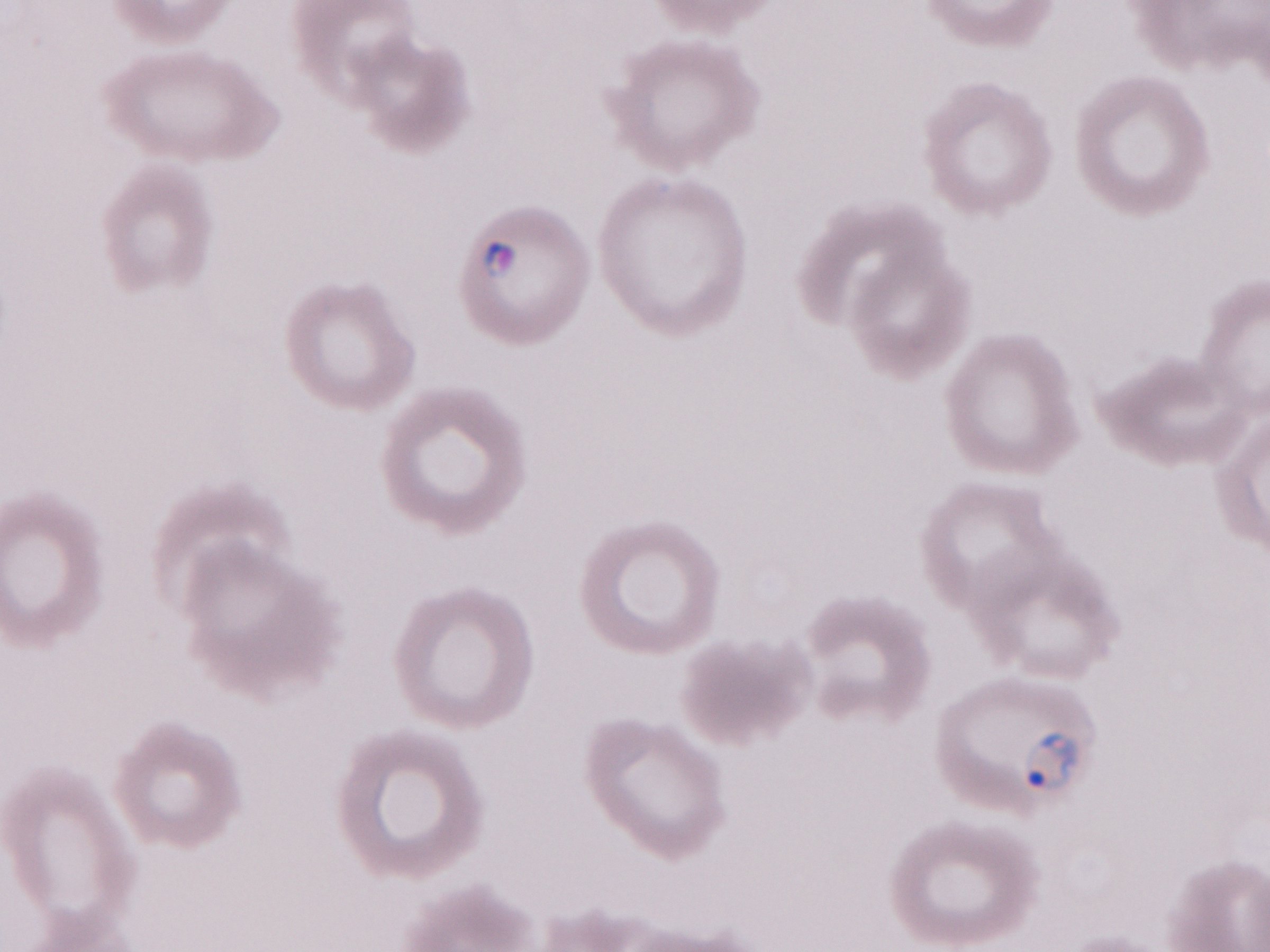 May-Grünwald-Giemsa (MGG) stain. Patient diagnosis: malaria infection. Olympus BX43 microscope and DP73 digital camera. One field of this slide. Thin blood film. Image is 1270×952 pixels. 1,000x magnification.